Locate every leukocyte (white blood cell).
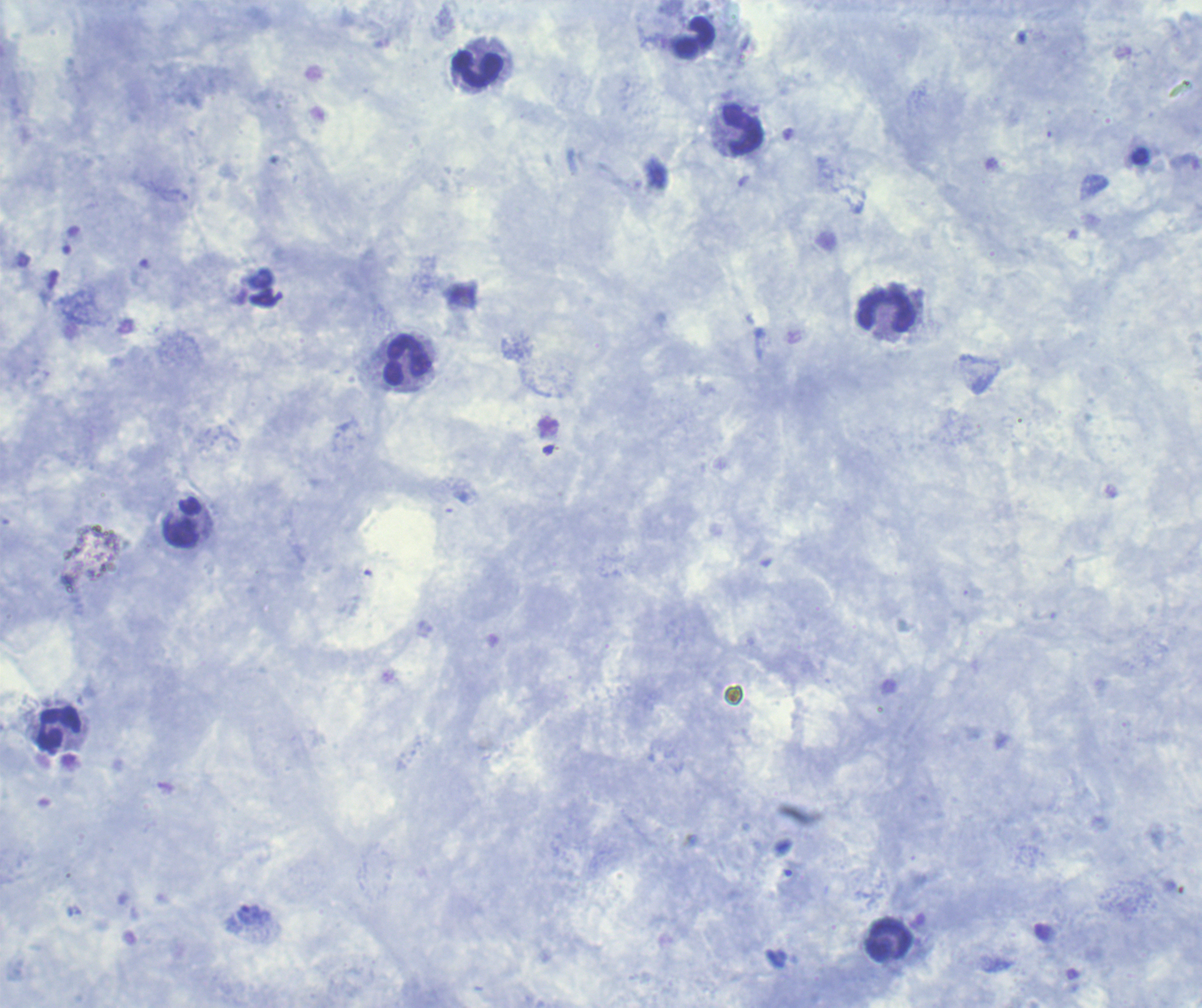

Approximate centers as (x, y) in pixels.
Leukocytes: (695, 38), (478, 68), (742, 129), (886, 310), (407, 360), (183, 523), (59, 727), (890, 939).

Approximate centers as (x, y) in pixels. Trophozoite locations: (252, 915). Single field of view. Romanowsky stain. Background quality: satisfactory. Previously used in a real diagnosis. Coloration quality: good. Result: positive for Plasmodium parasites. 100x magnification. Image is 1202×1008 pixels. Thick blood film.